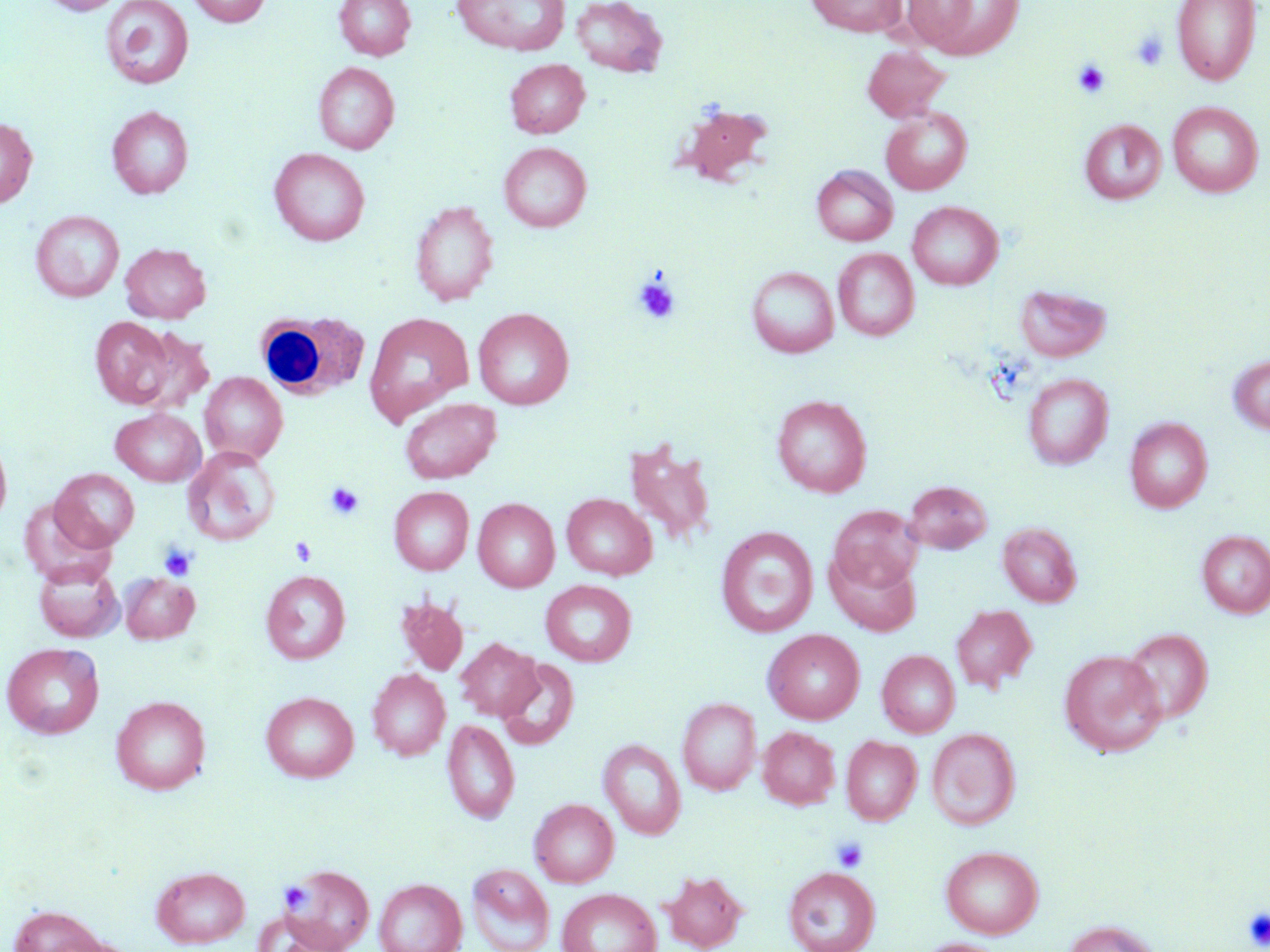
Summary:
  - Coordinate format: approximate bounding boxes as (x1,y1)-(x2,y2) corner pairs in pixels
  - White blood cell locations: (255,310)-(369,400)
  - Platelet locations: (1130,31)-(1169,71), (1073,59)-(1111,99), (633,277)-(681,325), (325,482)-(365,520), (290,537)-(317,566), (159,543)-(197,581), (832,837)-(868,872), (280,881)-(312,913), (1244,907)-(1270,949)
  - Uninfected red blood cell locations: (41,0)-(124,15), (186,0)-(271,27), (334,0)-(416,61), (452,0)-(570,55), (571,0)-(668,77), (805,0)-(908,36), (905,0)-(1024,59), (1171,0)-(1261,85), (100,1)-(194,89), (862,46)-(951,121), (505,59)-(589,138), (313,62)-(399,154), (1167,102)-(1264,197), (677,104)-(774,186), (107,106)-(193,199), (881,107)-(972,195), (0,116)-(37,208), (1079,119)-(1166,204), (499,142)-(591,232), (269,147)-(370,246), (812,165)-(898,246), (410,200)-(499,306), (908,200)-(1002,290), (30,210)-(124,302), (120,243)-(211,323), (833,248)-(919,341), (746,266)-(839,357), (1015,284)-(1111,362), (473,308)-(574,410), (363,311)-(474,425), (90,316)-(175,408), (130,328)-(216,416), (1228,354)-(1270,434), (200,372)-(288,463), (1023,373)-(1113,469), (771,394)-(872,497), (400,398)-(501,483), (110,408)-(206,486), (1125,418)-(1212,513), (0,432)-(12,530), (622,438)-(717,547), (182,447)-(280,545), (51,468)-(140,551), (903,479)-(992,554), (389,486)-(474,575), (562,493)-(656,580), (18,497)-(115,587), (473,498)-(559,592), (828,505)-(922,593), (998,522)-(1082,607), (715,526)-(818,638), (1197,529)-(1270,619), (825,548)-(922,636), (34,559)-(124,642), (261,570)-(350,664), (120,573)-(199,643), (540,579)-(637,666), (395,596)-(468,675), (950,604)-(1038,693), (1121,627)-(1213,723), (763,629)-(865,724), (456,638)-(542,721), (2,642)-(104,739), (877,649)-(961,737), (1058,649)-(1168,757), (497,658)-(579,751), (367,669)-(451,760), (261,691)-(358,782), (111,695)-(210,794), (678,697)-(761,795), (443,719)-(519,824), (758,726)-(840,809), (926,727)-(1021,830), (841,735)-(922,825), (599,739)-(686,840), (529,798)-(619,887), (939,846)-(1044,939), (284,863)-(375,952), (466,863)-(554,952), (151,865)-(250,948), (783,866)-(881,952), (661,869)-(748,952), (374,878)-(467,952), (557,888)-(661,952), (8,905)-(108,952), (1063,919)-(1162,952), (916,938)-(1009,952)
  - Slide-level diagnosis: no evidence of blood parasites
  - Magnification: 1000x
  - Preparation: thin blood film
  - Image size: 1270×952 pixels
  - Stain: May-Grünwald-Giemsa
  - Field of view: one of a larger specimen
  - Modality: optical microscopy